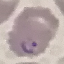
Malaria status: parasitized. Giemsa stain. Acquired by smartphone through the microscope eyepiece. Thin smear of blood. Cell patch, automatically extracted from a larger field of view and resized to 64 × 64 pixels.